Assess this cell for malaria.
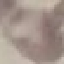
It is uninfected.

Thin blood film. Acquired by smartphone through the microscope eyepiece. Giemsa stain. Automatically extracted cell patch, resized to 64 × 64 pixels.